Give the position of every Plasmodium parasite visible.
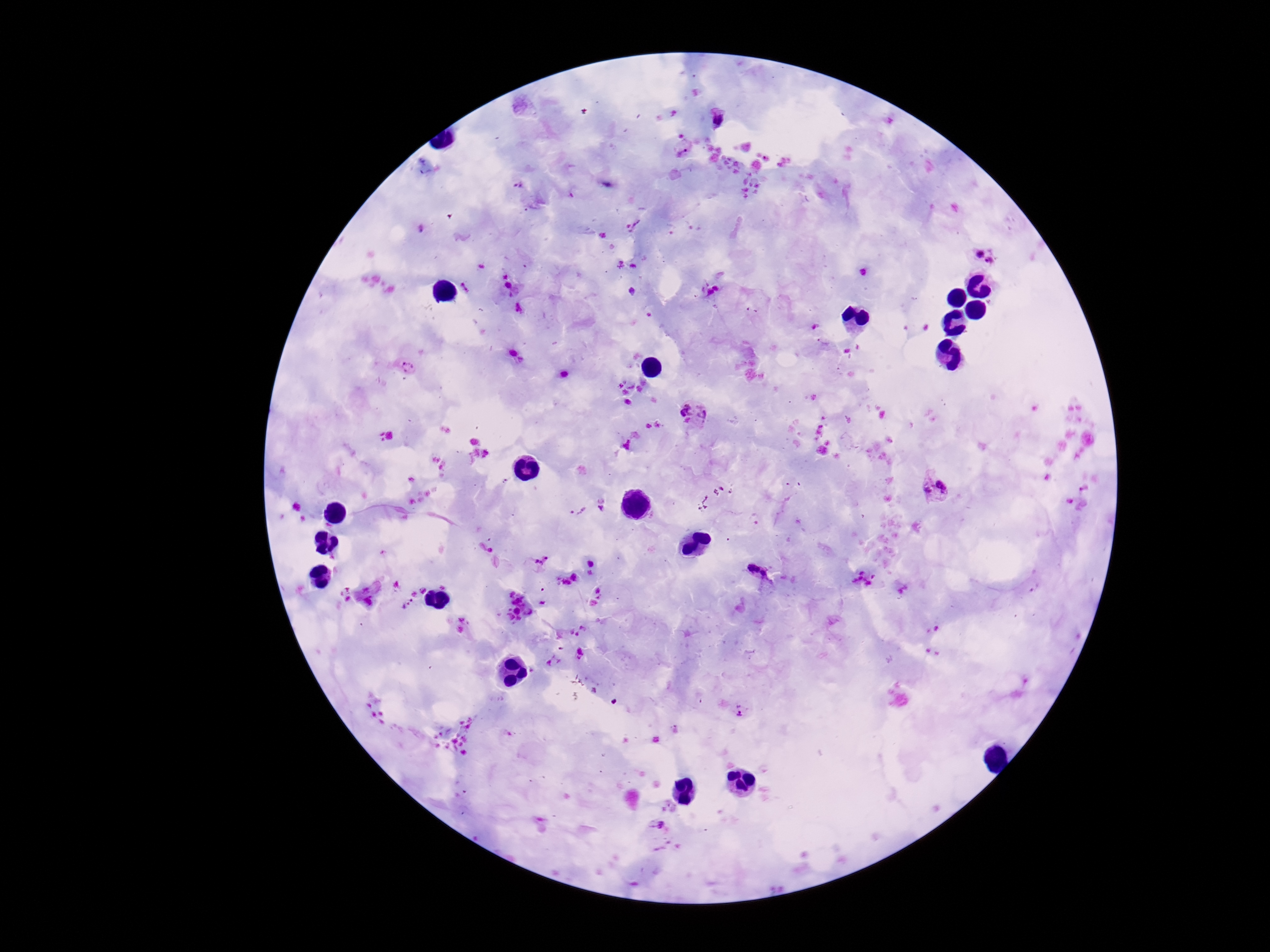

Approximate centers as {x, y} in pixels.
Plasmodium parasites: {718, 119}, {684, 147}, {519, 186}, {633, 226}, {986, 255}, {508, 282}, {709, 289}, {520, 309}, {404, 366}, {693, 415}, {936, 487}, {602, 506}, {577, 509}, {483, 547}, {534, 559}, {759, 570}, {862, 578}, {407, 602}, {579, 654}, {553, 660}, {740, 709}, {659, 825}.

Summary:
  - Capture: smartphone camera through the microscope eyepiece
  - Image size: 1270×952 pixels
  - Stain: Giemsa
  - Patient malaria status: positive
  - Field of view: one from this slide
  - Magnification: 100x
  - Preparation: thick peripheral-blood smear